Locate and identify every blood parasite.
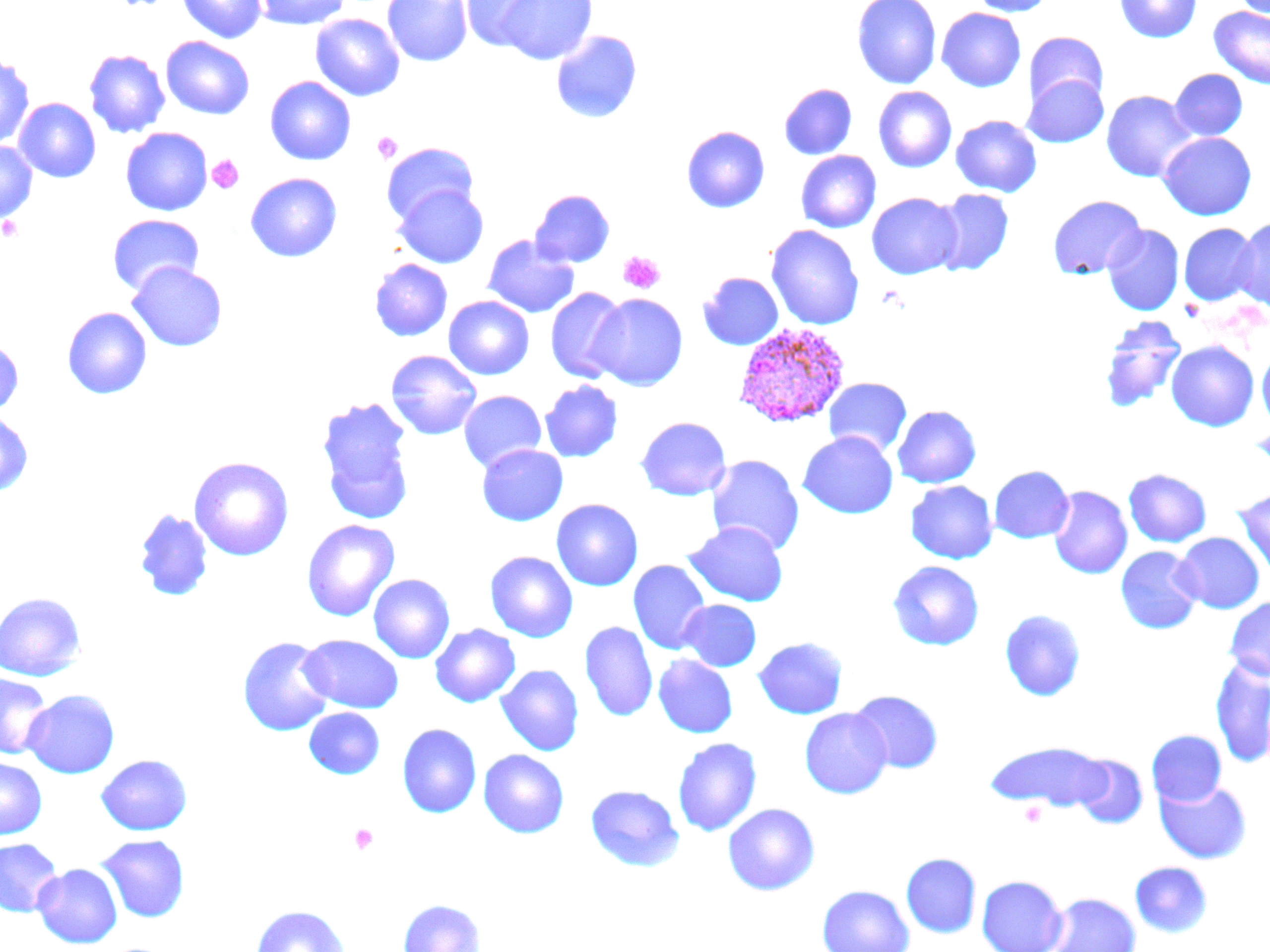
Approximate bounding boxes as [x1, y1, x2, y2] in pixels.
Plasmodium vivax-infected red blood cells: [732, 323, 850, 428].
No Plasmodium falciparum, Plasmodium ovale, Plasmodium malariae, Babesia divergens, or Trypanosoma brucei observed.

Uninfected red blood cell locations: [177, 0, 267, 44], [253, 0, 351, 29], [382, 0, 473, 67], [460, 0, 547, 52], [492, 0, 598, 65], [852, 0, 942, 89], [969, 0, 1056, 17], [1114, 0, 1202, 43], [1231, 0, 1270, 19], [1209, 6, 1270, 89], [936, 8, 1026, 92], [310, 13, 405, 101], [551, 30, 642, 123], [1024, 32, 1109, 110], [161, 36, 255, 120], [84, 49, 170, 138], [0, 56, 34, 150], [1170, 69, 1247, 141], [1022, 73, 1108, 148], [265, 76, 356, 165], [779, 83, 857, 159], [873, 86, 957, 173], [1101, 90, 1197, 182], [13, 98, 101, 183], [951, 115, 1042, 197], [681, 126, 770, 213], [121, 127, 212, 216], [1158, 132, 1257, 220], [0, 142, 37, 224], [381, 142, 479, 225], [796, 151, 881, 233], [245, 173, 342, 263], [393, 185, 488, 268], [530, 189, 615, 267], [932, 189, 1014, 276], [866, 193, 963, 280], [1047, 194, 1146, 279], [107, 215, 204, 295], [1233, 218, 1270, 310], [1178, 223, 1260, 305], [1102, 224, 1185, 315], [766, 225, 864, 330], [482, 235, 578, 318], [369, 259, 452, 342], [127, 262, 227, 352], [698, 272, 783, 351], [545, 287, 629, 384], [589, 293, 688, 391], [444, 296, 534, 380], [62, 306, 152, 400], [1099, 317, 1187, 412], [0, 338, 24, 417], [1165, 340, 1259, 431], [1257, 349, 1270, 431], [386, 350, 482, 440], [824, 378, 912, 457], [540, 380, 623, 463], [459, 391, 546, 473], [315, 395, 416, 525], [892, 405, 982, 487], [0, 412, 33, 496], [634, 416, 731, 501], [798, 431, 898, 519], [476, 444, 568, 525], [706, 455, 804, 556], [188, 456, 294, 561], [989, 465, 1074, 543], [1123, 468, 1212, 547], [906, 480, 997, 563], [1048, 486, 1132, 579], [1234, 487, 1270, 579], [551, 499, 643, 591], [134, 508, 213, 601], [301, 519, 401, 622], [684, 521, 788, 606], [1174, 532, 1265, 613], [1115, 546, 1203, 634], [485, 551, 578, 642], [628, 560, 711, 655], [887, 561, 984, 650], [368, 574, 455, 663], [0, 592, 87, 681], [1225, 597, 1270, 681], [677, 599, 761, 671], [999, 609, 1086, 702], [579, 620, 658, 722], [430, 624, 521, 707], [298, 634, 404, 713], [237, 636, 335, 736], [753, 637, 847, 718], [653, 654, 738, 738], [1210, 658, 1270, 767], [495, 664, 583, 755], [0, 672, 53, 759], [22, 689, 120, 778], [849, 690, 943, 774], [303, 707, 385, 780], [799, 707, 892, 798], [397, 723, 482, 818], [1147, 730, 1226, 806], [672, 737, 762, 837], [985, 741, 1112, 810], [478, 749, 569, 837], [1071, 753, 1148, 829], [96, 754, 192, 835], [0, 756, 47, 839], [1155, 779, 1251, 863], [584, 784, 684, 871], [723, 803, 820, 895], [95, 834, 190, 922], [0, 838, 63, 915], [901, 853, 981, 938], [1129, 861, 1213, 938], [32, 863, 123, 948], [901, 864, 1067, 942], [977, 874, 1067, 952], [817, 884, 914, 952], [1047, 892, 1140, 952], [398, 898, 486, 952], [251, 905, 351, 952]. Platelet locations: [372, 131, 402, 163], [207, 155, 244, 194], [0, 216, 23, 242], [618, 251, 665, 293], [1252, 424, 1270, 469], [1020, 801, 1047, 827], [349, 824, 378, 854]. Slide-level diagnosis: Plasmodium vivax. Image is 1270×952 pixels. Optical microscopy. 1000x magnification. One field of a larger specimen. Thin blood smear. May-Grünwald-Giemsa stain.